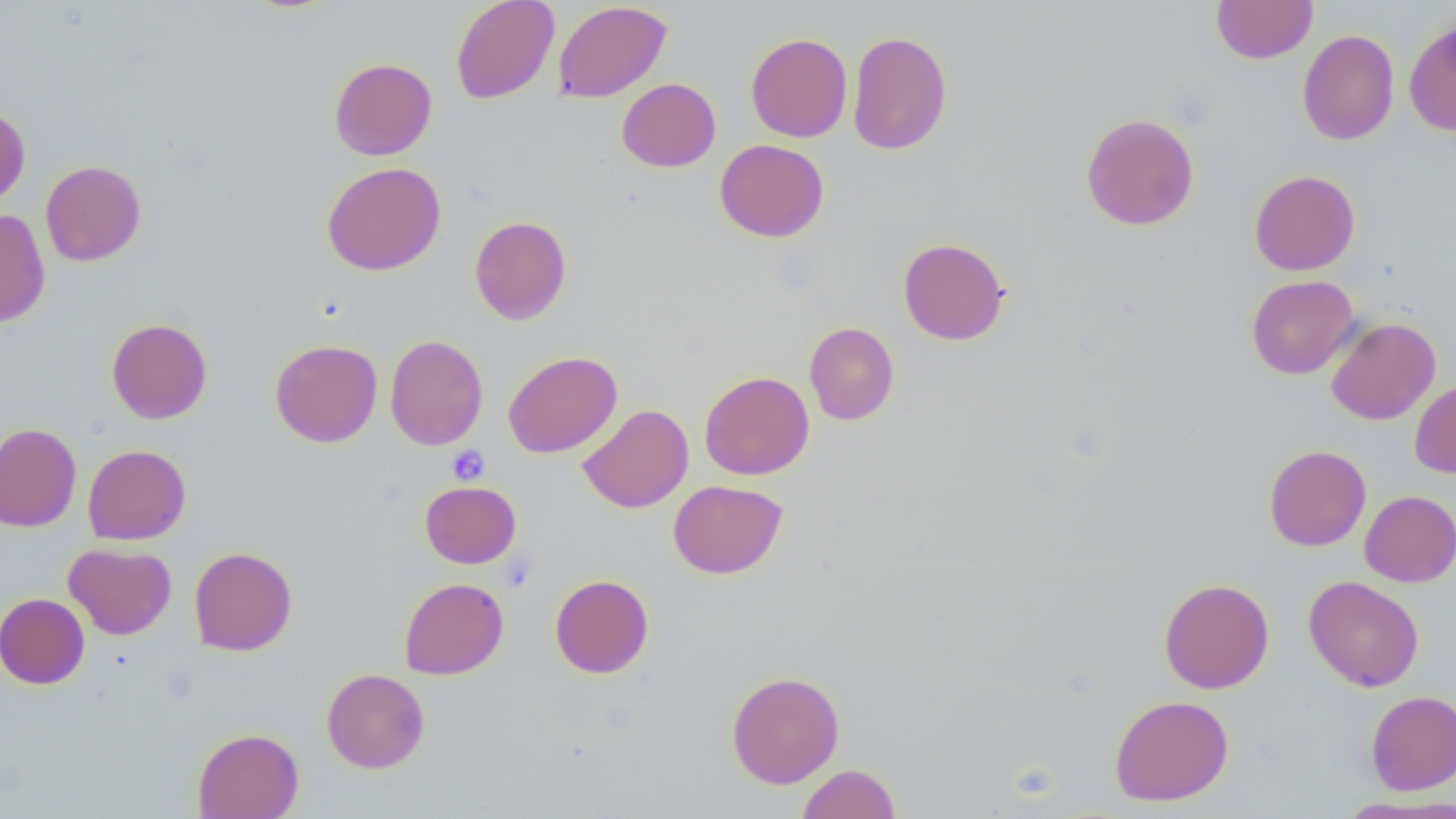
Approximate bounding boxes as (x1,y1)-(x2,y2) corner pairs in pixels. Uninfected red blood cell locations: (451,0)-(559,104), (1212,0)-(1317,63), (553,1)-(671,102), (1404,20)-(1456,137), (1297,29)-(1399,145), (847,30)-(952,156), (746,32)-(852,142), (329,58)-(437,161), (616,78)-(720,172), (0,105)-(31,207), (1081,113)-(1200,230), (715,139)-(829,242), (40,160)-(146,266), (322,162)-(446,276), (1249,170)-(1360,275), (0,208)-(50,326), (469,215)-(572,325), (898,237)-(1009,345), (1246,275)-(1359,379), (1326,317)-(1441,424), (106,318)-(212,424), (804,322)-(899,425), (385,335)-(488,450), (270,339)-(382,447), (503,350)-(622,458), (699,370)-(814,480), (1410,379)-(1456,478), (578,404)-(693,513), (0,422)-(81,532), (83,444)-(191,544), (1264,445)-(1371,551), (668,479)-(787,579), (420,480)-(521,568), (1359,490)-(1456,587), (63,542)-(177,640), (189,546)-(297,655), (550,574)-(654,678), (1304,576)-(1424,691), (399,577)-(509,679), (1159,577)-(1274,694), (0,593)-(90,689), (321,668)-(430,773), (726,670)-(845,788), (1366,690)-(1456,795), (1109,694)-(1234,806), (192,727)-(304,819), (797,763)-(901,819), (1335,795)-(1456,817). Platelet locations: (446,444)-(489,485). Slide-level diagnosis: no evidence of blood parasites. Single field of view. May-Grünwald-Giemsa-stained preparation. Optical microscopy. Thin blood smear. Image is 1456×819 pixels. 1000x magnification.